Locate every Plasmodium parasite.
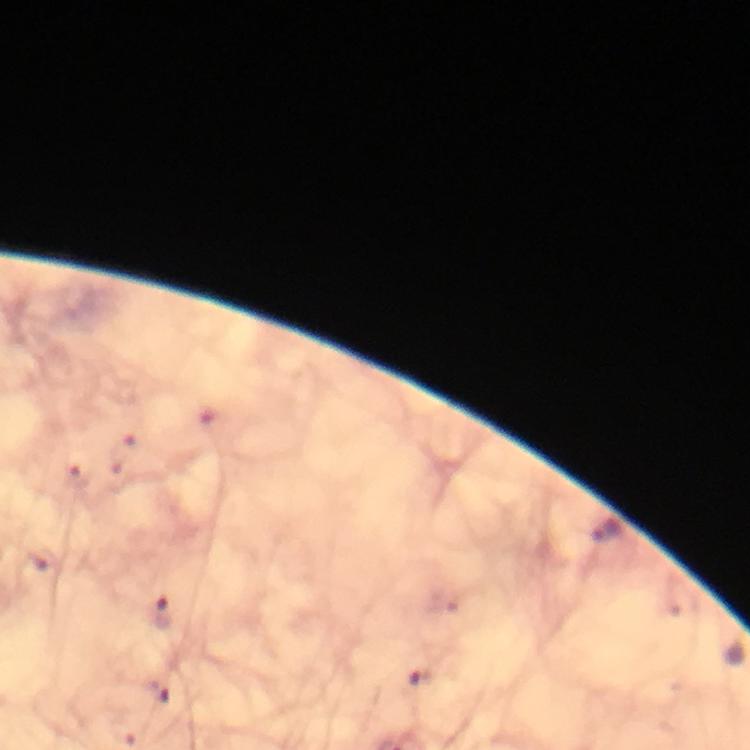
Approximate object centers, in pixels from the top-left corner.
Plasmodium parasites: (x=164, y=614).

preparation = thick blood film
image size = 750×750 pixels
stain = Giemsa
capture = smartphone photograph through a microscope
immersion oil = applied
context = from a diagnostic examination for malaria
magnification = 100x
cropped from = a single field of view